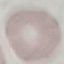

Summary:
  - Malaria status: uninfected
  - Capture: smartphone camera at the microscope eyepiece
  - Image type: cell patch, automatically extracted from a larger field of view and resized to 64 × 64 pixels
  - Stain: Giemsa
  - Preparation: thin smear